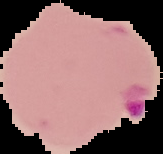
image type = cell region segmented out of the field of view; surrounding area masked to black
preparation = thin blood smear
image size = 163×154 pixels
malaria status = parasitized